Name the parasite shown.
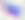
Toxoplasma gondii.

Summary:
  - Magnification: 400x
  - Modality: micrograph